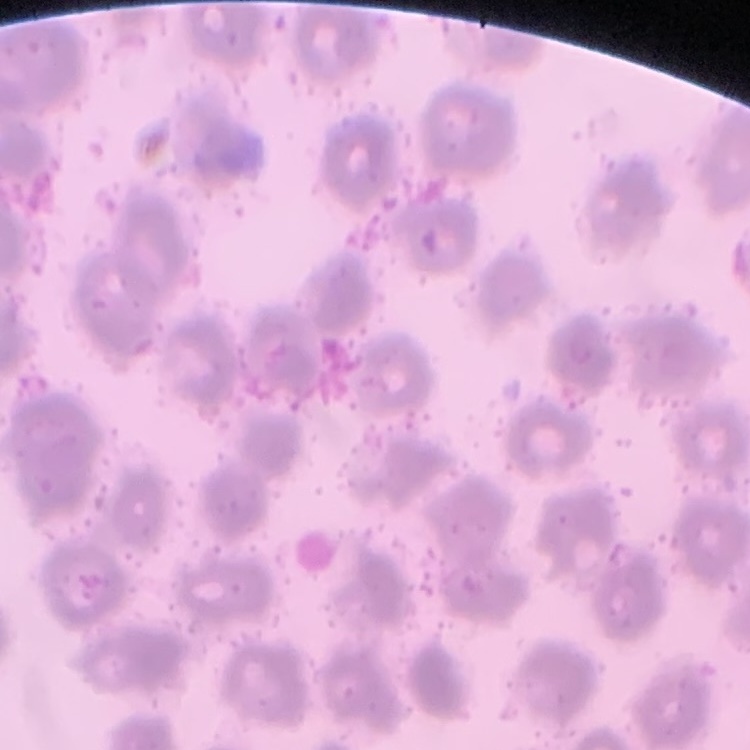

erythrocyte morphology = no rouleaux formation
image type = one tile cut from a larger photomicrograph
stain = Field's or Giemsa
preparation = thin blood smear